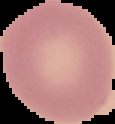
preparation = thin blood smear
image size = 115×124 pixels
image type = segmented cell region on a black background
malaria status = uninfected